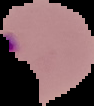

preparation = thin blood smear
result = malaria parasites identified
image size = 94×106 pixels
image type = segmented cell region with the area outside set to black